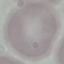
Result: negative for malaria parasites. Giemsa stain. Cell patch, automatically extracted from a larger field of view and resized to 64 × 64 pixels. Thin blood film. Acquired by smartphone through the microscope eyepiece.